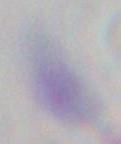
Micrograph. 1000x magnification. Toxoplasma gondii is shown.